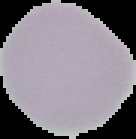

Summary:
  - Result: negative for malaria parasites
  - Image size: 136×139 pixels
  - Preparation: thin blood smear
  - Image type: segmented cell region on a black background